Identify the parasite.
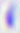
This is Toxoplasma gondii.

magnification = 400x
modality = micrograph